Classify this cell by malaria status.
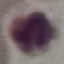
It is uninfected.

preparation: thin smear
capture: smartphone through the microscope eyepiece
stain: Giemsa
image_type: cell patch, automatically extracted from a larger field of view and resized to 64 × 64 pixels